Assess this cell for malaria.
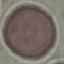
Uninfected.

Summary:
  - Stain: Giemsa
  - Preparation: thin blood smear
  - Capture: smartphone through the microscope eyepiece
  - Image type: automatically extracted cell patch, resized to 64 × 64 pixels